Assess this cell for malaria.
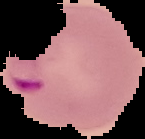
Parasitized.

preparation: thin blood smear
image_type: segmented cell region on a black background
image_size: 145×139 pixels